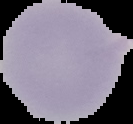
Segmented cell region on a black background. From a thin blood smear. Image is 133×124 pixels. Result: negative for Plasmodium parasites.